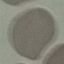 Malaria status: uninfected. Photographed with a smartphone camera at the microscope eyepiece. Automatically extracted cell patch, resized to 64 × 64 pixels. Thin blood smear. Giemsa-stained preparation.